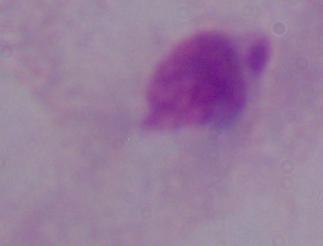

A trichomonad is shown. Photomicrograph. Captured at 1000x magnification.